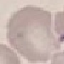
malaria status = uninfected
stain = Giemsa
capture = smartphone through the microscope eyepiece
preparation = thin blood film
image type = cell patch, automatically extracted from a larger field of view and resized to 64 × 64 pixels